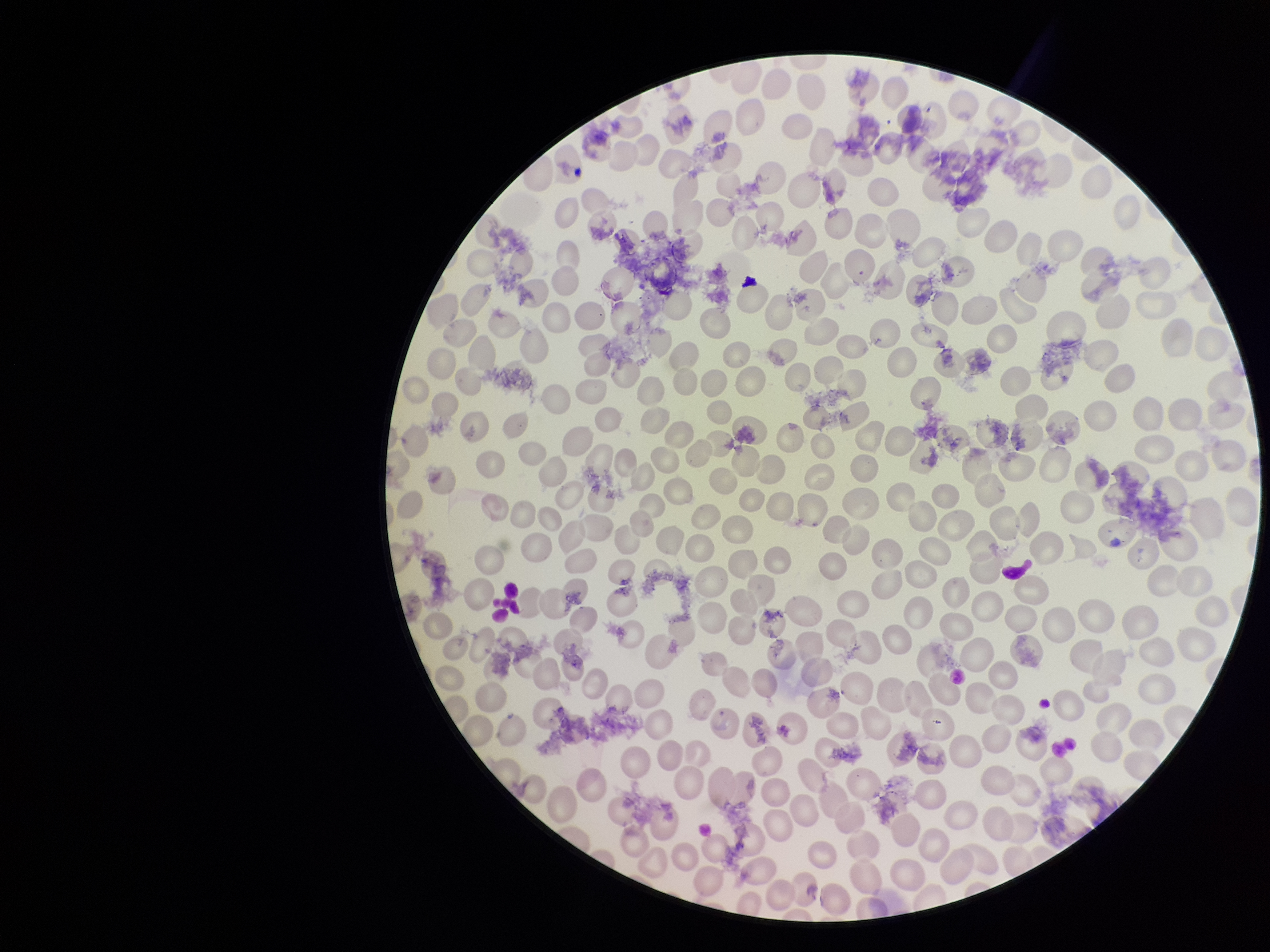
stain = Giemsa
parasitized red blood cell count = 0
image size = 1270×952 pixels
parasitized red blood cells = none seen
capture = smartphone photograph through the microscope eyepiece
species reported for this patient = Plasmodium falciparum
red blood cell count = 230
preparation = thin smear
patient malaria status = infected
field of view = single